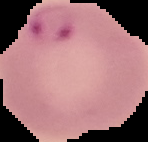

Summary:
  - Preparation: thin blood film
  - Image type: segmented cell region with the area outside set to black
  - Result: malaria parasites identified
  - Image size: 148×142 pixels